Outline each Plasmodium malariae-infected red blood cell.
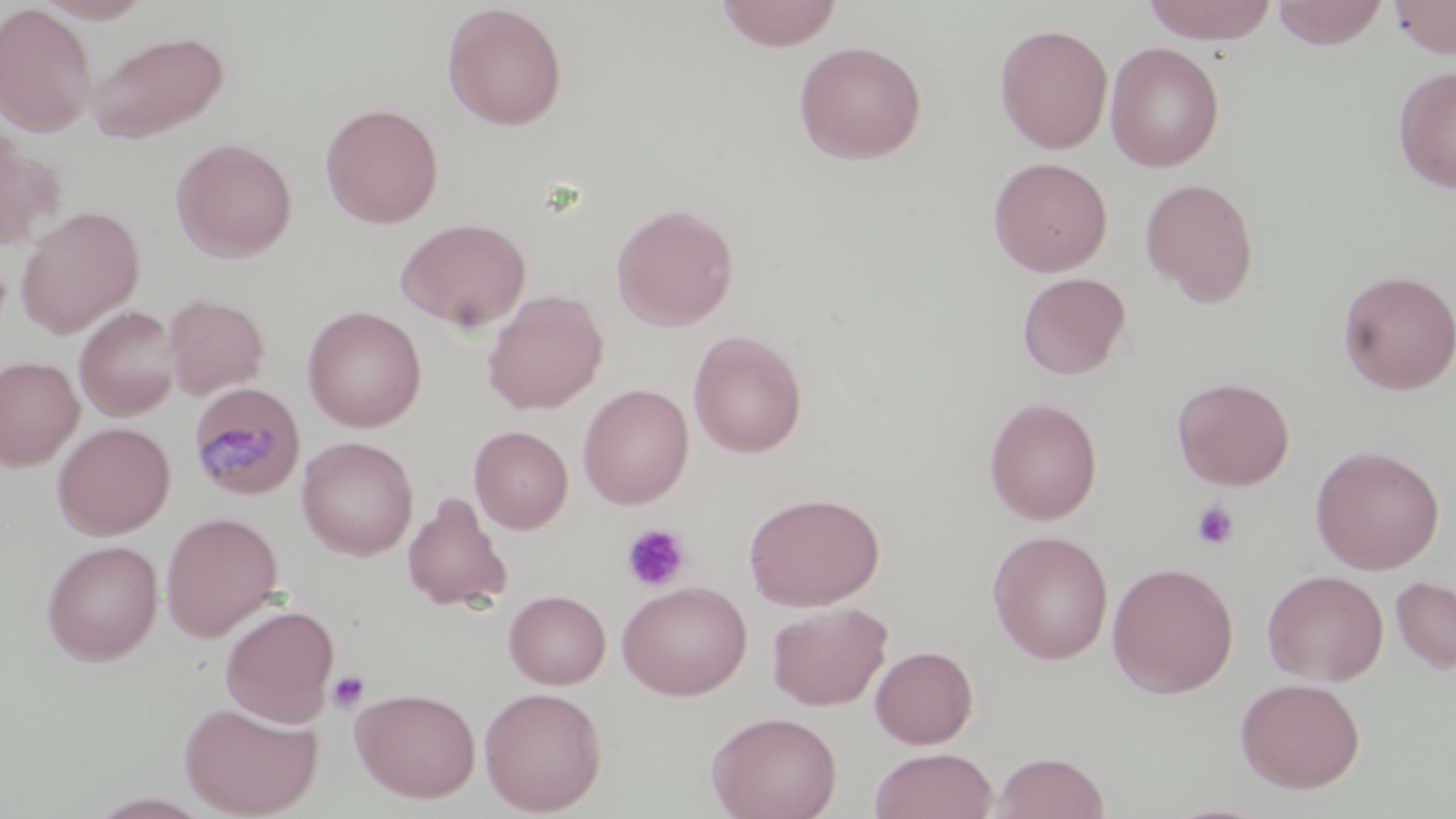
Approximate bounding boxes as (x1,y1)-(x2,y2) corner pairs in pixels.
Plasmodium malariae-infected red blood cells: (187,381)-(306,501).

Summary:
  - Uninfected red blood cell locations: (35,0)-(152,23), (714,0)-(843,51), (1141,0)-(1278,45), (1271,0)-(1390,48), (1388,0)-(1456,58), (442,2)-(569,131), (0,4)-(98,137), (994,22)-(1113,153), (85,29)-(230,143), (792,40)-(928,165), (1104,41)-(1224,172), (1393,65)-(1456,194), (320,102)-(444,228), (0,123)-(56,250), (171,137)-(297,262), (988,156)-(1113,276), (1139,177)-(1260,305), (611,203)-(739,331), (16,206)-(144,338), (396,217)-(532,333), (1337,269)-(1456,395), (1016,272)-(1132,380), (483,289)-(608,415), (162,293)-(271,400), (74,305)-(181,421), (302,305)-(427,432), (688,330)-(808,458), (0,355)-(84,471), (1172,376)-(1296,490), (578,383)-(694,509), (984,396)-(1103,524), (52,421)-(175,539), (469,425)-(573,533), (297,436)-(418,560), (1310,444)-(1445,574), (744,490)-(885,610), (402,491)-(513,612), (161,511)-(282,641), (988,529)-(1114,664), (42,539)-(163,665), (1107,561)-(1239,698), (1262,569)-(1388,685), (1390,575)-(1456,674), (617,580)-(752,700), (504,590)-(611,688), (768,602)-(891,710), (220,604)-(340,726), (869,645)-(979,748), (1235,676)-(1366,793), (351,686)-(481,803), (478,686)-(608,816), (179,700)-(323,817), (706,710)-(842,819), (869,747)-(997,819), (990,750)-(1111,819)
  - Platelet locations: (1191,500)-(1239,551), (621,523)-(690,592), (327,670)-(369,713)
  - Slide-level diagnosis: Plasmodium malariae
  - Modality: optical microscopy
  - Preparation: thin blood smear
  - Field of view: single
  - Image size: 1456×819 pixels
  - Stain: May-Grünwald-Giemsa
  - Magnification: 1000x